Assess this cell for malaria.
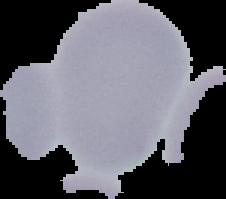
It is uninfected.

Summary:
  - Image type: segmented cell region on a black background
  - Image size: 226×199 pixels
  - Preparation: thin blood film